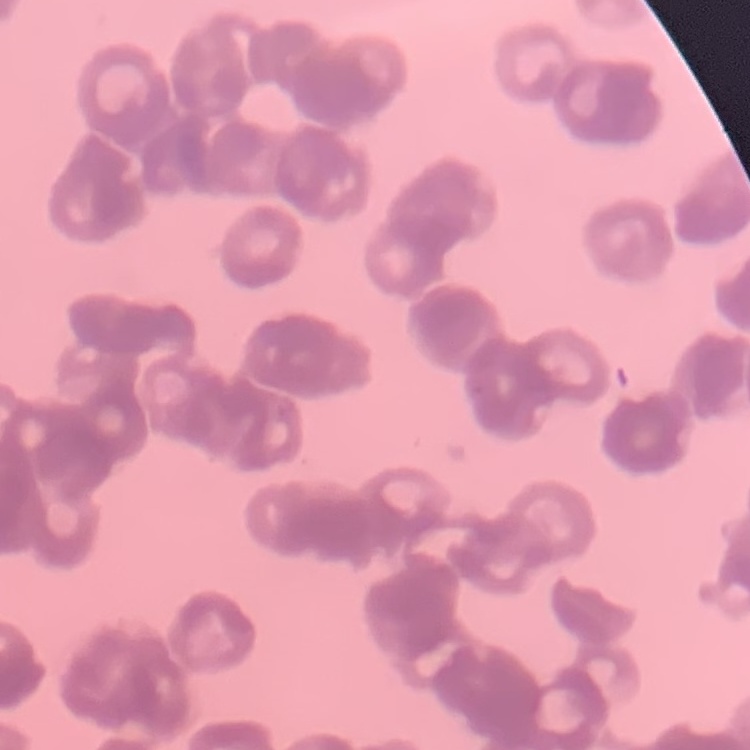

{
  "red_blood_cell_morphology": "rouleaux formation",
  "image_type": "square crop of a larger photomicrograph",
  "preparation": "thin peripheral smear",
  "stain": "Field's or Giemsa"
}